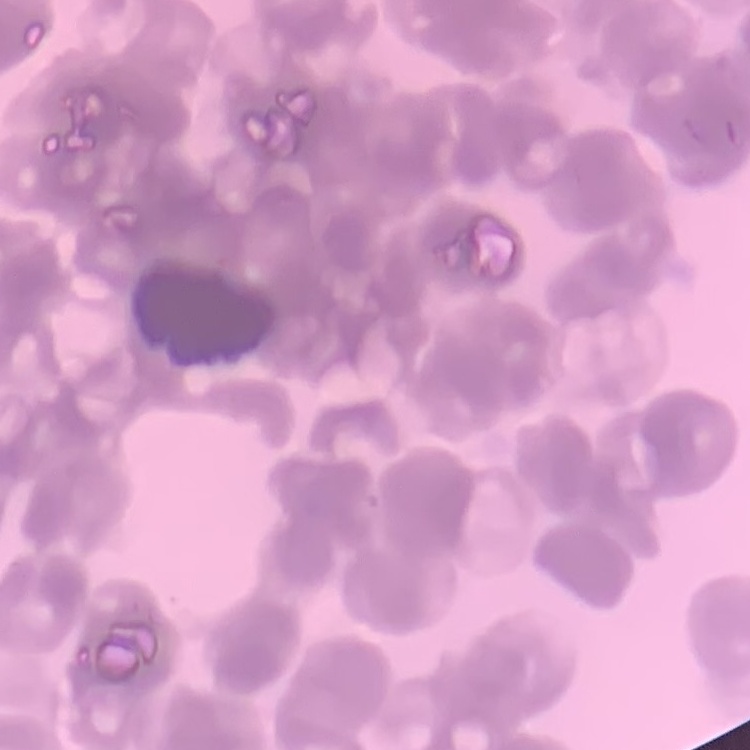

Summary:
  - Red blood cell morphology: rouleaux formation
  - Stain: Field's or Giemsa
  - Image type: square crop of a larger photomicrograph
  - Preparation: thin blood smear